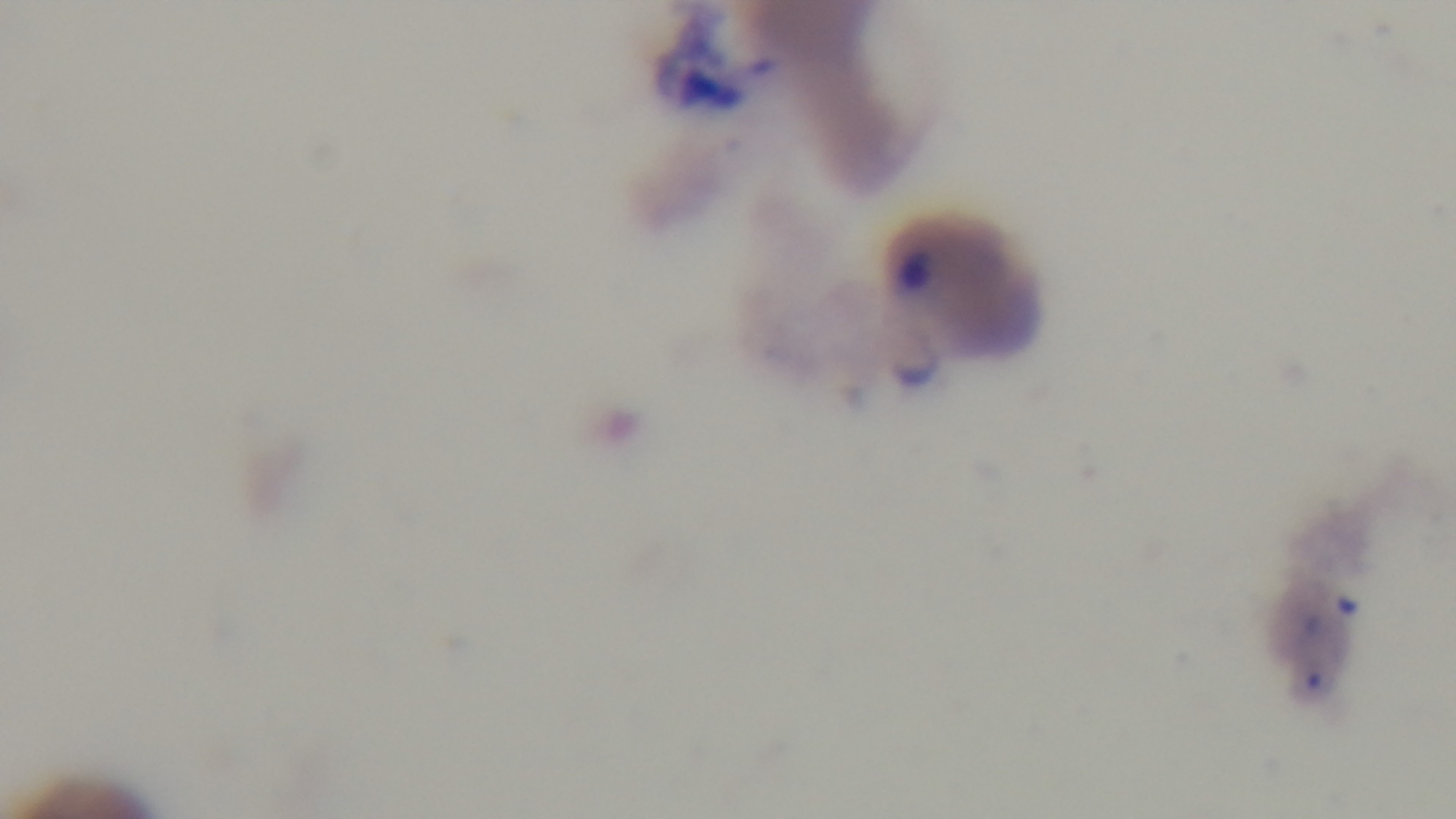
preparation: thin blood film
field_of_view: single
objective: 100x oil immersion
capture: mounted 4K digital camera
malaria_status: positive
modality: light microscopy
stain: Giemsa